State which parasite is depicted.
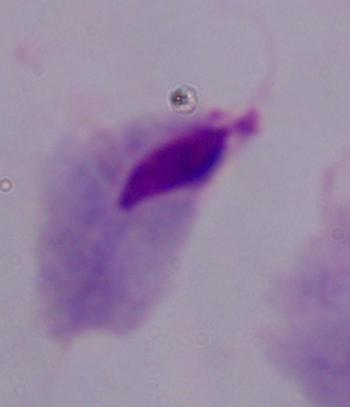
This is a trichomonad.

magnification = 1000x
modality = photomicrograph